State which parasite is depicted.
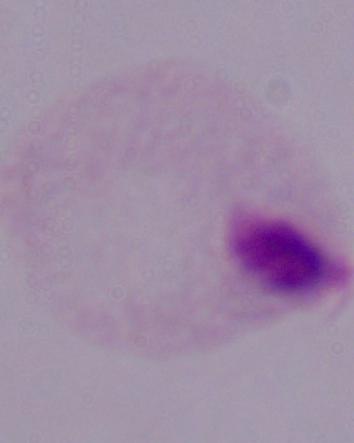
This is a trichomonad.

Summary:
  - Modality: photomicrograph
  - Magnification: 1000x